Locate every blood parasite and identify its species.
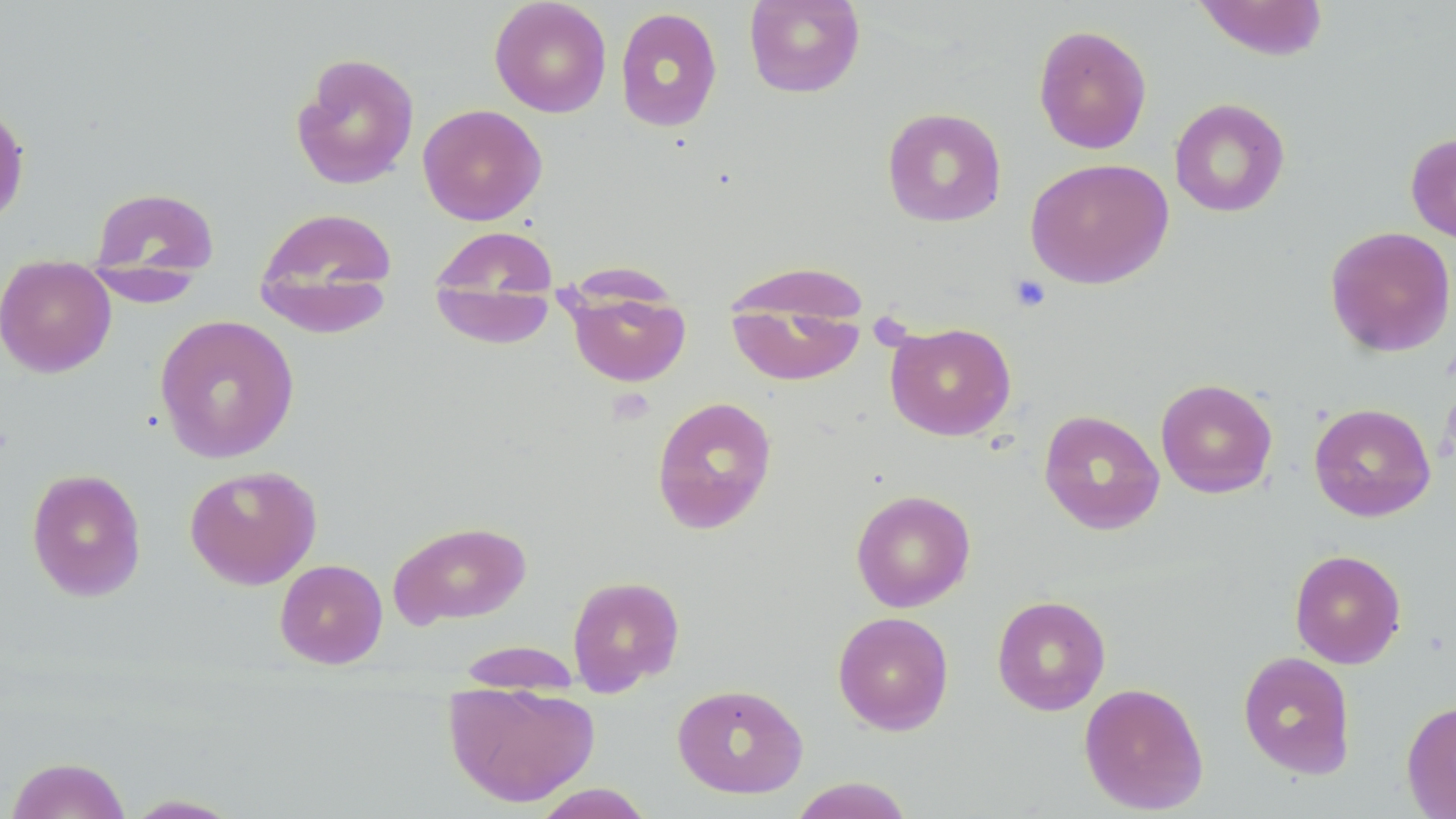

No blood parasites seen.

Approximate bounding boxes as (x1,y1)-(x2,y2) corner pairs in pixels. Platelet locations: (1009,274)-(1051,312). Uninfected red blood cell locations: (489,0)-(612,118), (743,0)-(865,98), (1193,0)-(1330,61), (615,7)-(723,133), (1032,24)-(1152,154), (291,52)-(420,190), (1169,98)-(1290,217), (0,100)-(31,228), (417,104)-(547,225), (881,107)-(1007,227), (1405,132)-(1456,244), (1025,157)-(1174,289), (87,186)-(220,281), (254,207)-(398,327), (429,225)-(560,322), (1325,226)-(1456,357), (1,255)-(116,378), (722,260)-(873,327), (84,264)-(203,307), (428,267)-(558,348), (564,290)-(692,387), (726,297)-(866,386), (154,314)-(300,464), (886,321)-(1016,441), (1155,378)-(1278,498), (651,395)-(778,534), (1309,402)-(1436,522), (1038,409)-(1165,534), (184,464)-(322,589), (26,468)-(147,601), (850,489)-(976,612), (388,520)-(532,628), (1290,549)-(1406,668), (274,559)-(388,669), (566,574)-(685,695), (992,595)-(1111,715), (833,611)-(954,735), (454,639)-(583,691), (1237,651)-(1356,778), (442,681)-(600,808), (1079,682)-(1209,815), (672,683)-(809,798), (1401,699)-(1456,818), (6,756)-(132,819), (787,777)-(915,819), (530,783)-(656,818), (122,794)-(245,818). Slide-level diagnosis: no evidence of blood parasites. 1000x magnification. Optical microscopy. May-Grünwald-Giemsa-stained preparation. Thin blood film. Single field of view. Image is 1456×819 pixels.